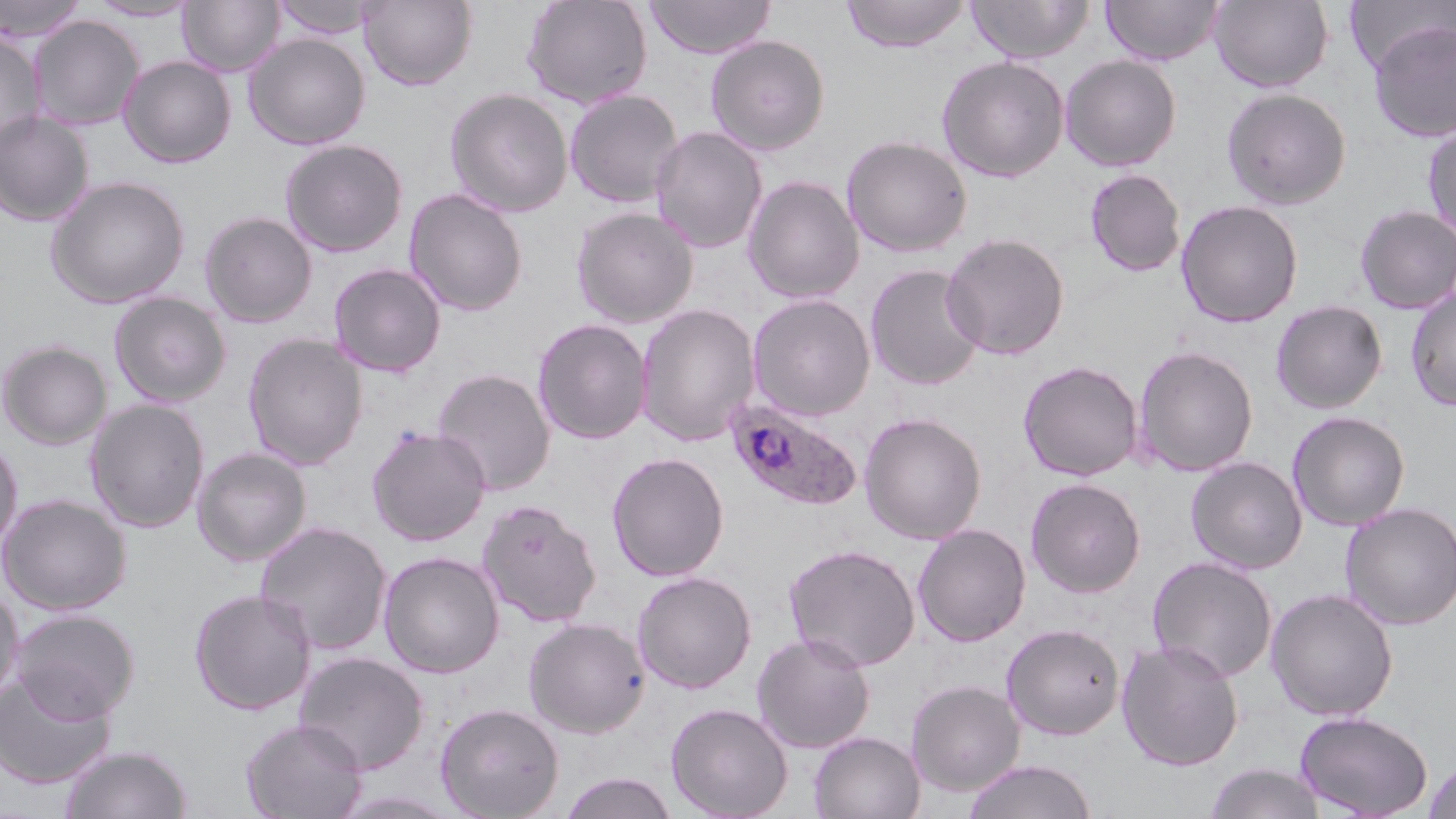

slide_level_diagnosis: Plasmodium ovale
modality: light microscopy
plasmodium_ovale_infected_red_blood_cell_locations: 'approximate bounding boxes as (x1,y1)-(x2,y2) corner pairs in pixels: (724,396)-(864,512)'
image_size: 1456×819 pixels
stain: May-Grünwald-Giemsa
preparation: thin blood smear
uninfected_red_blood_cell_locations: 'approximate bounding boxes as (x1,y1)-(x2,y2) corner pairs in pixels: (0,0)-(87,43), (178,0)-(283,77), (270,0)-(381,40), (359,0)-(478,91), (521,0)-(653,110), (644,0)-(776,59), (841,0)-(972,52), (968,0)-(1093,63), (1101,0)-(1224,66), (1209,0)-(1333,92), (87,1)-(199,21), (1346,1)-(1454,77), (28,15)-(144,130), (1367,19)-(1456,143), (0,30)-(47,152), (244,33)-(370,150), (705,34)-(830,155), (1060,54)-(1181,171), (118,55)-(237,168), (937,55)-(1069,182), (445,87)-(574,217), (1221,87)-(1352,210), (564,89)-(684,208), (0,111)-(94,226), (1422,121)-(1456,245), (650,125)-(768,253), (840,134)-(973,257), (279,138)-(409,257), (1085,168)-(1187,277), (45,175)-(191,309), (743,175)-(865,303), (403,188)-(529,317), (1176,199)-(1303,328), (1353,204)-(1456,314), (571,206)-(699,328), (199,211)-(318,328), (940,232)-(1070,360), (328,263)-(446,377), (865,263)-(985,391), (1405,286)-(1456,412), (109,292)-(232,408), (747,293)-(876,421), (1270,300)-(1387,414), (635,304)-(761,446), (532,318)-(652,445), (242,333)-(368,470), (0,340)-(113,450), (1132,345)-(1259,476), (1018,360)-(1143,481), (432,368)-(556,495), (85,398)-(210,533), (1287,410)-(1410,531), (859,412)-(987,544), (366,425)-(491,546), (0,437)-(23,555), (192,447)-(312,566), (607,452)-(729,581), (1186,456)-(1307,574), (1025,477)-(1146,597), (0,493)-(131,615), (477,499)-(602,628), (1339,501)-(1456,630), (255,521)-(393,655), (912,524)-(1031,647), (783,543)-(920,672), (378,551)-(505,678), (1146,555)-(1278,683), (631,570)-(757,693), (0,583)-(24,708), (189,588)-(317,715), (1265,588)-(1399,721), (10,608)-(139,722), (523,617)-(650,737), (1001,623)-(1125,740), (752,632)-(875,754), (1116,639)-(1244,771), (294,651)-(430,774), (0,671)-(116,788), (906,679)-(1025,796), (435,702)-(565,819), (665,702)-(793,819), (1293,710)-(1433,818), (240,717)-(368,819), (808,731)-(925,818), (60,744)-(193,819), (1423,758)-(1456,819), (962,759)-(1098,819), (1204,763)-(1326,819), (559,772)-(679,819), (328,789)-(467,818)'
magnification: 1000x
field_of_view: single